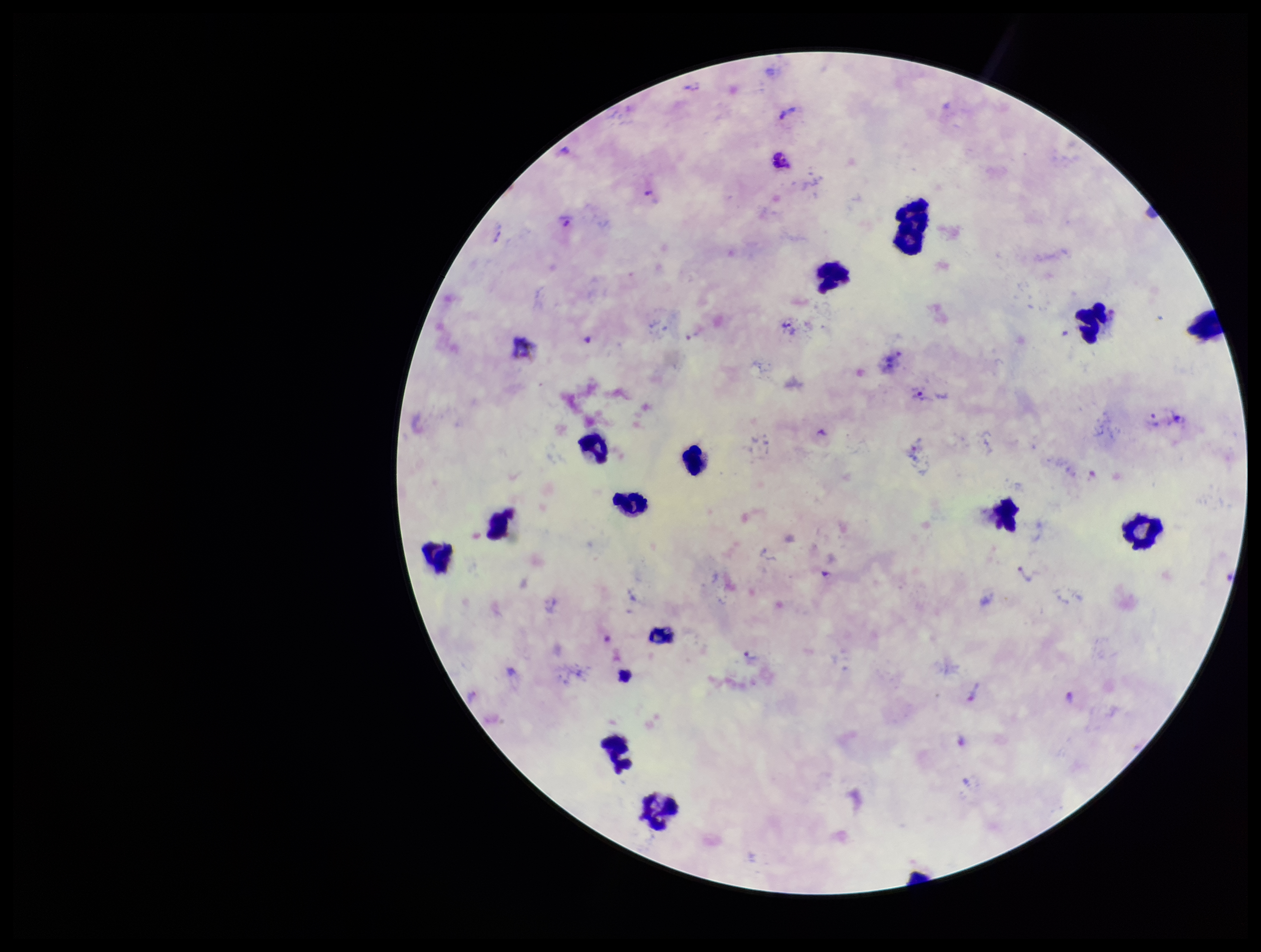

Summary:
  - Species reported for this patient: Plasmodium vivax
  - Patient malaria status: infected
  - Parasite count: 16
  - Image size: 1261×952 pixels
  - Capture: smartphone photograph through the microscope eyepiece
  - Stain: Giemsa
  - Preparation: thick blood smear
  - Field of view: one from this slide
  - Plasmodium parasites: seen
  - Leukocyte count: 14